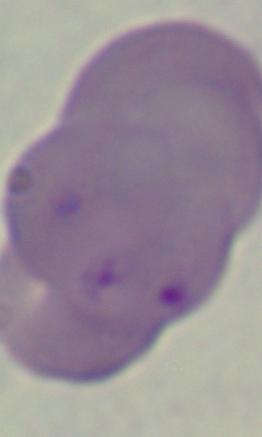
{
  "magnification": "1000x",
  "modality": "micrograph",
  "identification": "Babesia"
}